Identify the parasite.
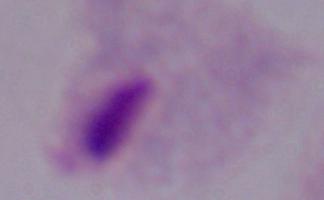

This is a trichomonad.

1000x magnification. Photomicrograph.